Assess this cell for malaria.
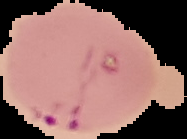

Parasitized.

Summary:
  - Preparation: thin blood film
  - Image type: cell region segmented out of the field of view; surrounding area masked to black
  - Image size: 187×139 pixels